State which parasite is depicted.
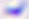

Toxoplasma gondii.

magnification = 400x
modality = photomicrograph